Outline each Plasmodium falciparum-infected red blood cell.
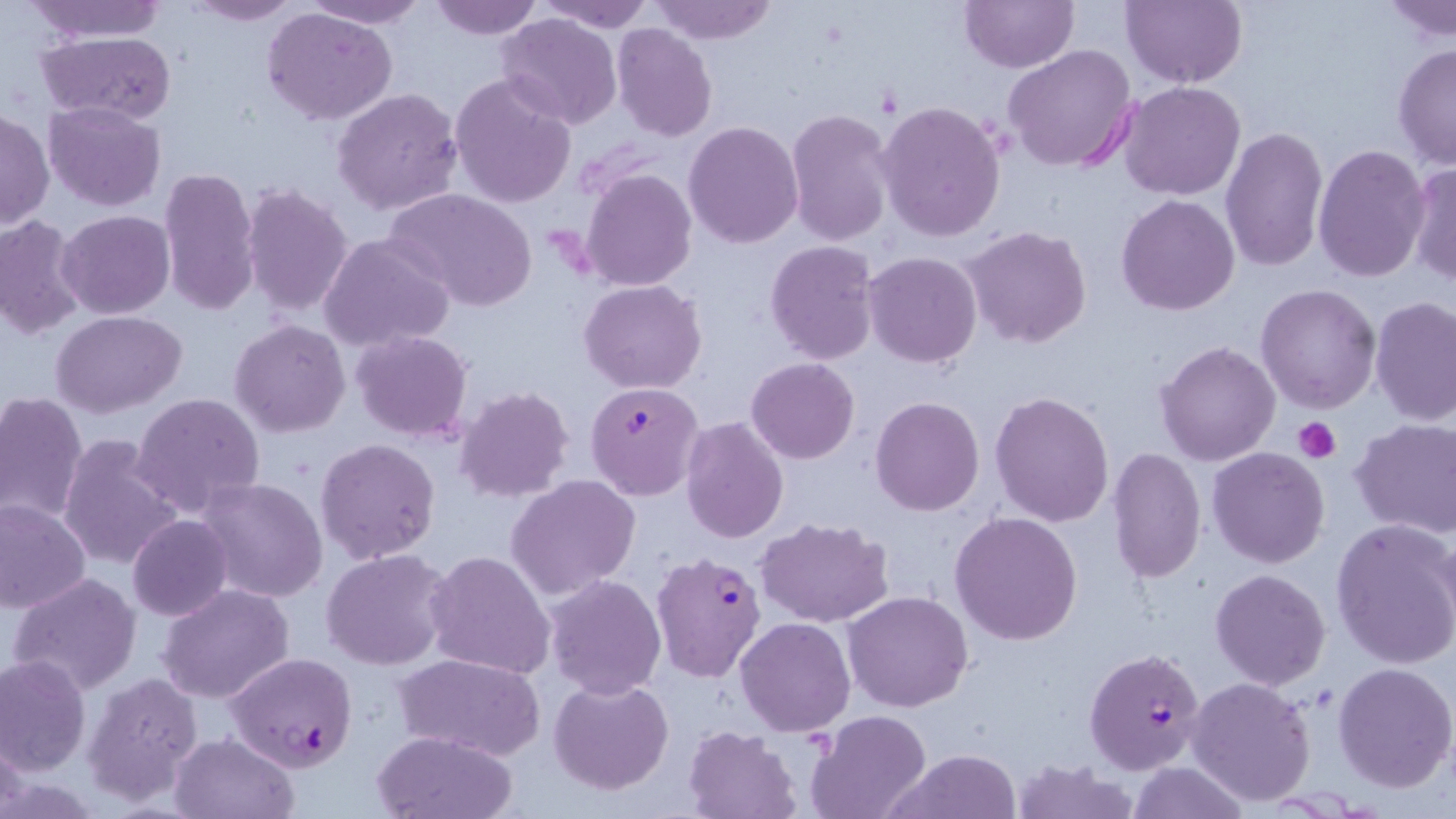
Approximate bounding boxes as (x1,y1)-(x2,y2) corner pairs in pixels.
Plasmodium falciparum-infected red blood cells: (584,381)-(703,501), (652,552)-(766,683), (1085,646)-(1207,776), (226,651)-(359,771).

Platelet locations: (1294,418)-(1342,464). Uninfected red blood cell locations: (300,0)-(430,27), (426,0)-(543,40), (537,0)-(657,32), (650,0)-(777,44), (959,0)-(1077,72), (1120,0)-(1247,89), (23,1)-(175,43), (180,1)-(305,26), (1383,1)-(1456,46), (262,7)-(397,125), (497,12)-(621,130), (612,24)-(718,143), (35,32)-(177,123), (1392,44)-(1455,171), (1004,45)-(1137,173), (450,73)-(578,210), (1117,81)-(1246,201), (331,87)-(463,216), (876,100)-(1006,242), (43,102)-(166,211), (787,108)-(897,249), (1,109)-(54,230), (683,120)-(802,248), (1220,125)-(1328,272), (1314,145)-(1430,283), (1406,162)-(1456,286), (580,167)-(697,291), (158,168)-(261,315), (241,183)-(355,319), (385,189)-(538,313), (1117,194)-(1238,316), (58,209)-(175,319), (0,215)-(87,340), (962,226)-(1092,349), (320,233)-(457,351), (765,240)-(880,364), (864,251)-(981,367), (580,279)-(706,393), (1255,284)-(1381,414), (1370,296)-(1456,426), (51,309)-(186,418), (228,318)-(351,438), (351,330)-(473,442), (1155,339)-(1281,466), (747,357)-(859,464), (453,386)-(576,503), (988,389)-(1114,527), (0,392)-(87,526), (132,392)-(266,518), (870,396)-(985,516), (681,416)-(788,541), (1350,420)-(1456,538), (58,434)-(182,570), (315,438)-(440,566), (1207,446)-(1329,569), (1107,448)-(1206,584), (506,475)-(641,599), (195,477)-(329,604), (0,500)-(91,615), (950,511)-(1083,646), (126,515)-(233,622), (757,517)-(895,626), (1330,518)-(1456,669), (321,548)-(456,670), (426,549)-(555,681), (1209,568)-(1331,691), (8,572)-(143,696), (543,573)-(667,699), (158,582)-(295,702), (844,591)-(973,713), (736,617)-(855,737), (395,652)-(545,759), (0,654)-(91,774), (1332,660)-(1456,792), (82,673)-(203,805), (1186,676)-(1316,807), (548,677)-(674,793), (805,711)-(930,819), (683,726)-(800,818), (0,727)-(27,817), (373,729)-(519,819), (170,733)-(298,819), (895,749)-(1022,819), (1010,758)-(1139,819), (1127,761)-(1247,818). Slide-level diagnosis: Plasmodium falciparum. Thin blood smear. May-Grünwald-Giemsa-stained preparation. Image is 1456×819 pixels. Single field of view. Light microscopy. Captured at 1000x magnification.